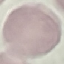
{
  "result": "no malaria parasites detected",
  "stain": "Giemsa",
  "capture": "smartphone through the microscope eyepiece",
  "preparation": "thin blood smear",
  "image_type": "automatically extracted cell patch, resized to 64 × 64 pixels"
}